Report the malaria status of this cell.
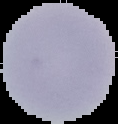

Uninfected.

Summary:
  - Image type: segmented cell region with the area outside set to black
  - Preparation: thin blood smear
  - Image size: 118×124 pixels